Name the cell type shown.
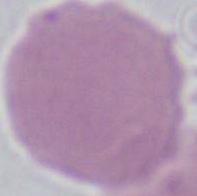
An erythrocyte.

magnification = 1000x
modality = photomicrograph